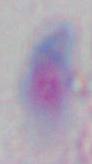
Summary:
  - Magnification: 1000x
  - Modality: photomicrograph
  - Identification: Toxoplasma gondii